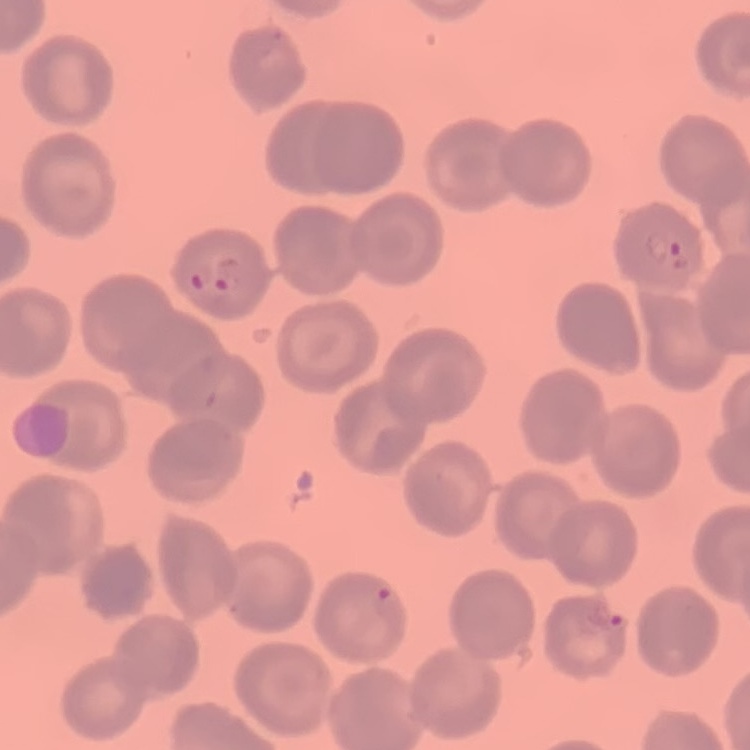
red blood cell morphology = no rouleaux formation
preparation = thin blood film
image type = one tile cut from a larger photomicrograph
stain = Field's or Giemsa